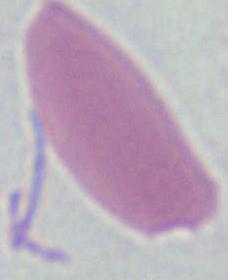

{
  "identification": "red blood cell",
  "modality": "photomicrograph",
  "magnification": "1000x"
}